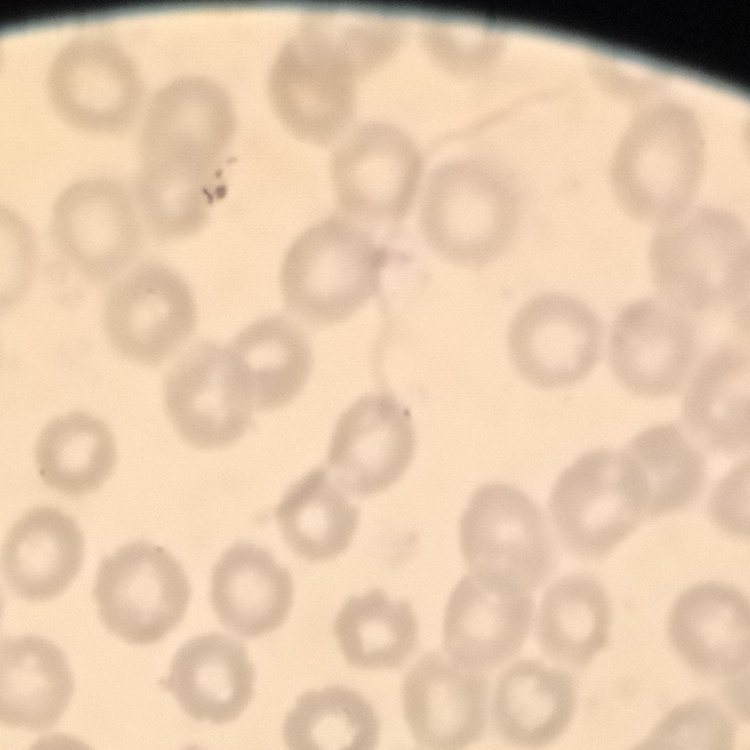

The red blood cells exhibit no rouleaux formation. One tile cut from a larger photomicrograph. Stained with either Field's or Giemsa. Thin peripheral smear.